Point out each Plasmodium parasite.
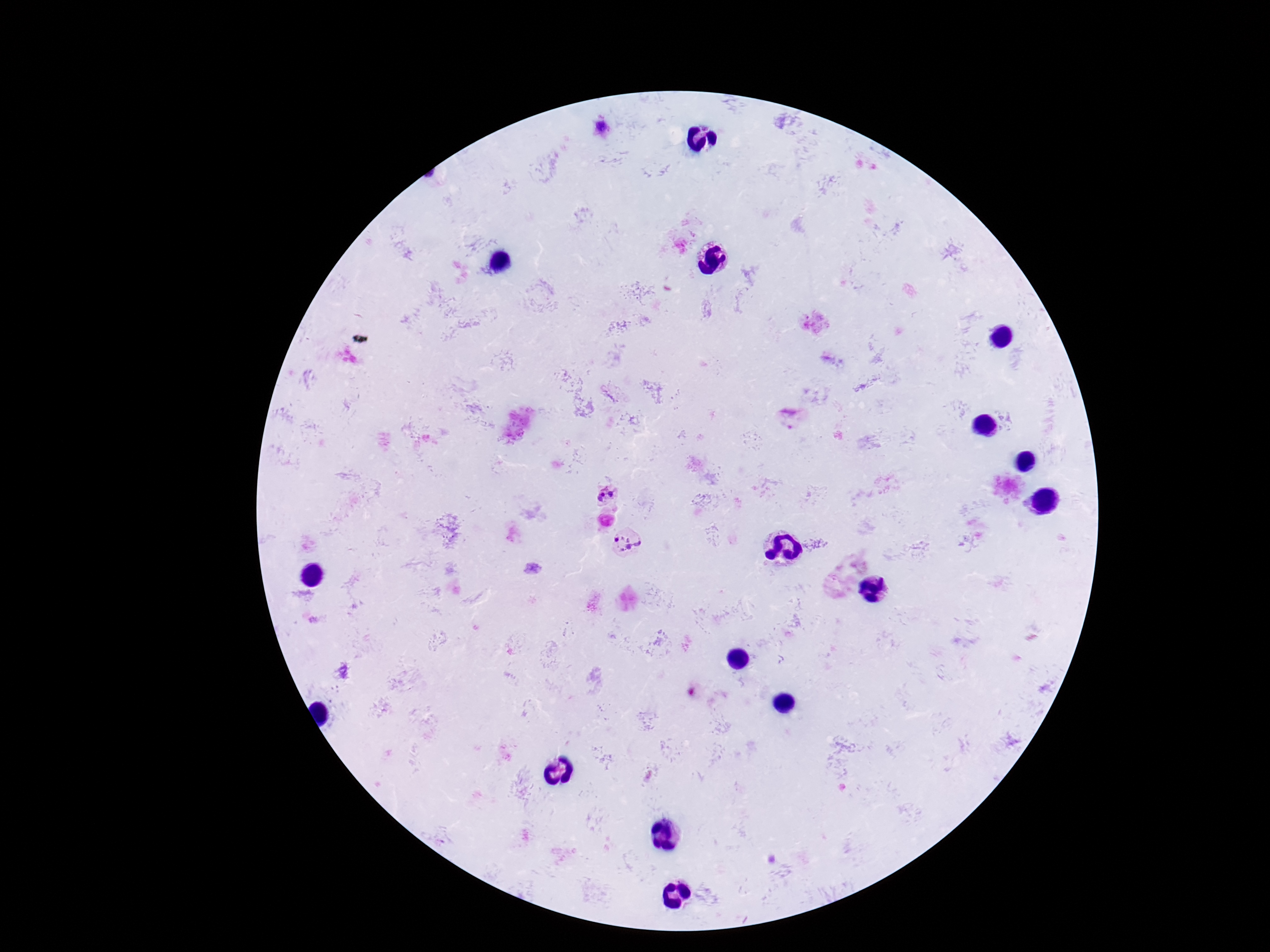

Approximate object centers, in pixels from the top-left corner.
Plasmodium parasites: (x=600, y=126), (x=792, y=416), (x=606, y=490), (x=628, y=543).

One field from this slide. Image is 1270×952 pixels. Patient malaria status: infected. Giemsa-stained preparation. Thick peripheral-blood smear. 100x magnification. Smartphone photograph taken through the microscope eyepiece.